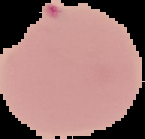
Summary:
  - Image size: 145×139 pixels
  - Image type: cell region segmented out of the field of view; surrounding area masked to black
  - Malaria status: parasitized
  - Preparation: thin blood smear